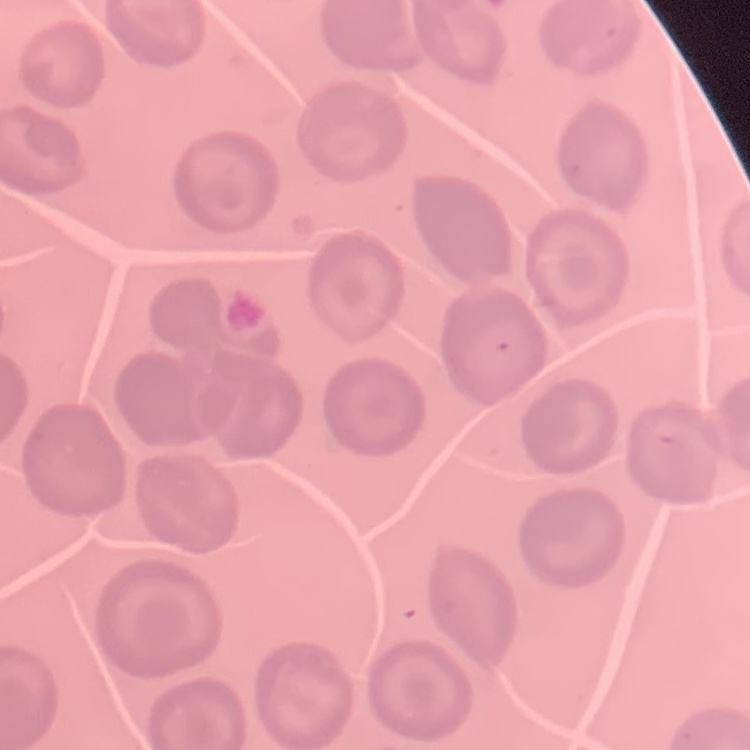
red blood cell morphology = no rouleaux formation
preparation = thin peripheral smear
image type = one tile cut from a larger photomicrograph
stain = Field's or Giemsa